Classify this cell by malaria status.
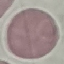
It is uninfected.

Summary:
  - Preparation: thin blood film
  - Stain: Giemsa
  - Image type: automatically extracted cell patch, resized to 64 × 64 pixels
  - Capture: smartphone camera at the microscope eyepiece